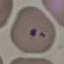
result = malaria parasites identified
preparation = thin blood film
capture = smartphone camera at the microscope eyepiece
image type = cell patch, automatically extracted from a larger field of view and resized to 64 × 64 pixels
stain = Giemsa